Assess this cell for malaria.
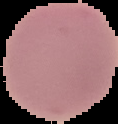

It is uninfected.

Summary:
  - Preparation: thin blood film
  - Image type: segmented cell region on a black background
  - Image size: 118×124 pixels